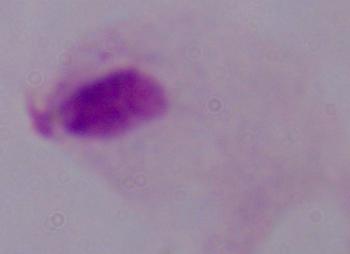

Summary:
  - Modality: photomicrograph
  - Identification: trichomonad
  - Magnification: 1000x